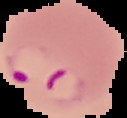

Summary:
  - Image size: 127×118 pixels
  - Malaria status: parasitized
  - Preparation: thin blood smear
  - Image type: cell region segmented out of the field of view; surrounding area masked to black